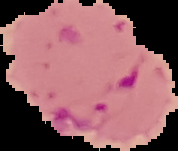
result: malaria parasites detected
preparation: thin blood film
image_size: 178×151 pixels
image_type: segmented cell region on a black background